Describe the morphology of the erythrocytes.
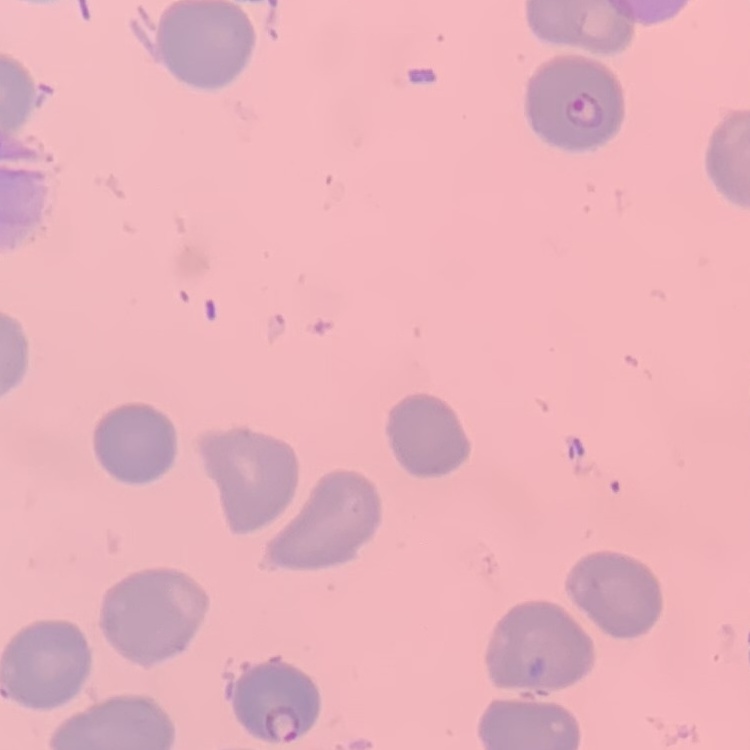
They show no rouleaux formation.

image type = square crop of a larger photomicrograph
preparation = thin peripheral smear
stain = Field's or Giemsa